Identify the parasite.
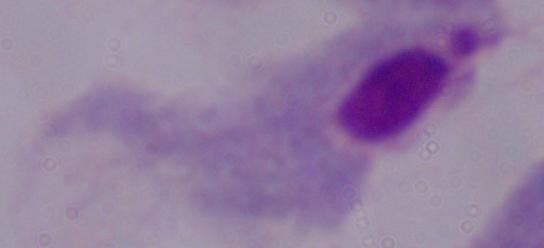

This is a trichomonad.

Summary:
  - Magnification: 1000x
  - Modality: photomicrograph